Report the malaria status of this cell.
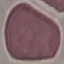
Uninfected.

preparation = thin smear
image type = automatically extracted cell patch, resized to 64 × 64 pixels
capture = smartphone camera at the microscope eyepiece
stain = Giemsa